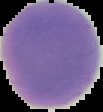
Summary:
  - Image size: 103×112 pixels
  - Malaria status: uninfected
  - Preparation: thin blood smear
  - Image type: segmented cell region on a black background